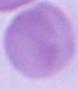

{
  "modality": "micrograph",
  "magnification": "1000x",
  "identification": "red blood cell"
}